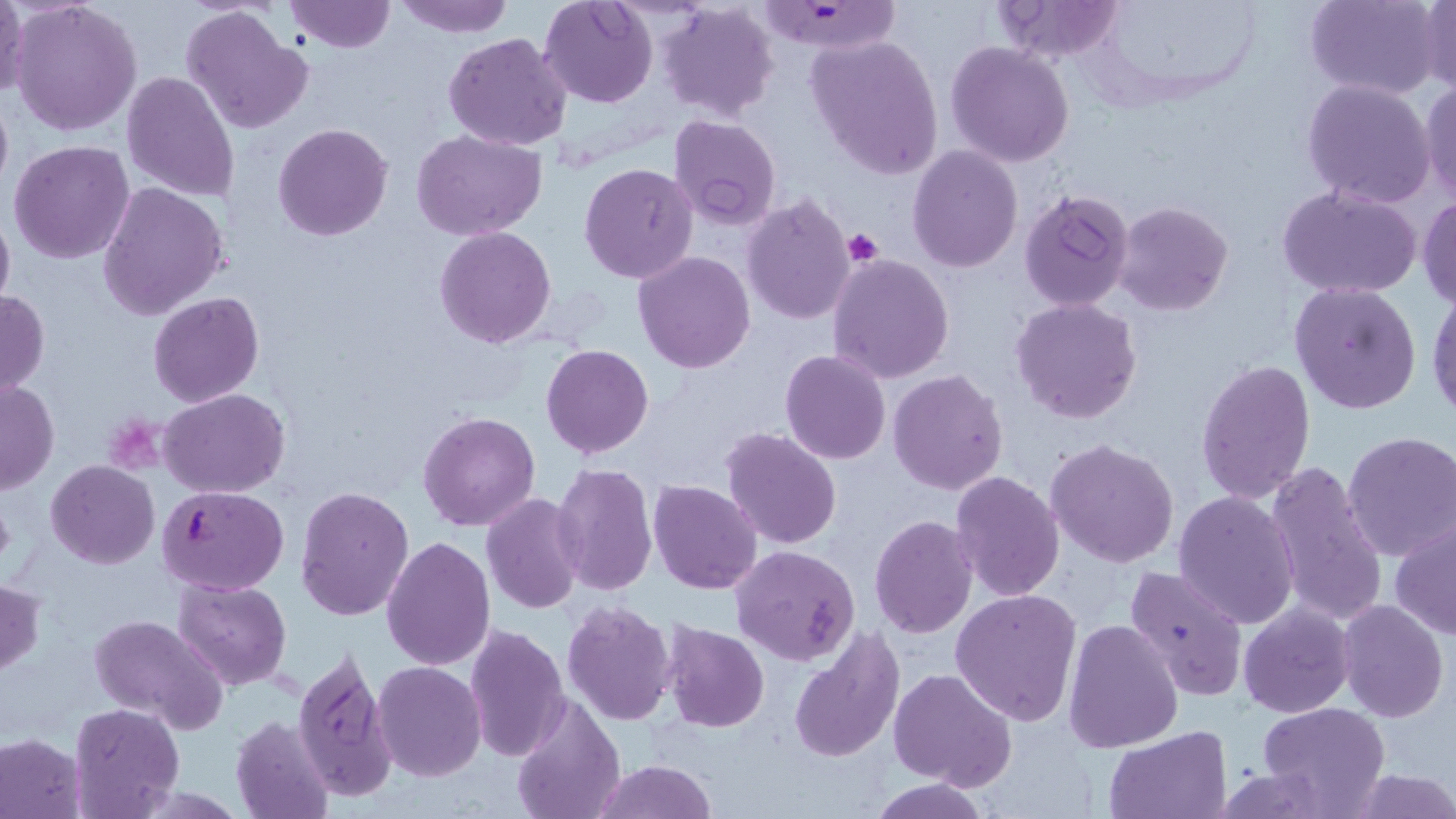
Summary:
  - Coordinate format: approximate bounding boxes as named x1/y1/x2/y2 corners in pixels
  - Plasmodium falciparum-infected red blood cell locations: (x1=755, y1=3, x2=906, y2=55), (x1=158, y1=485, x2=289, y2=595)
  - Platelet locations: (x1=843, y1=230, x2=883, y2=267)
  - Uninfected red blood cell locations: (x1=0, y1=0, x2=29, y2=101), (x1=9, y1=0, x2=142, y2=138), (x1=283, y1=0, x2=395, y2=53), (x1=394, y1=0, x2=513, y2=38), (x1=538, y1=0, x2=659, y2=109), (x1=992, y1=0, x2=1128, y2=62), (x1=1305, y1=0, x2=1443, y2=99), (x1=657, y1=1, x2=780, y2=121), (x1=1418, y1=1, x2=1455, y2=94), (x1=178, y1=7, x2=313, y2=135), (x1=443, y1=33, x2=572, y2=151), (x1=806, y1=34, x2=945, y2=179), (x1=946, y1=42, x2=1075, y2=168), (x1=122, y1=72, x2=240, y2=203), (x1=1302, y1=78, x2=1438, y2=207), (x1=1419, y1=79, x2=1456, y2=205), (x1=0, y1=83, x2=13, y2=201), (x1=668, y1=115, x2=781, y2=231), (x1=273, y1=123, x2=392, y2=241), (x1=598, y1=124, x2=746, y2=249), (x1=411, y1=128, x2=548, y2=240), (x1=8, y1=141, x2=133, y2=264), (x1=906, y1=146, x2=1024, y2=273), (x1=579, y1=162, x2=701, y2=283), (x1=98, y1=182, x2=228, y2=322), (x1=1276, y1=184, x2=1423, y2=300), (x1=1019, y1=188, x2=1135, y2=312), (x1=740, y1=192, x2=856, y2=325), (x1=1417, y1=195, x2=1456, y2=308), (x1=1113, y1=200, x2=1233, y2=315), (x1=0, y1=207, x2=14, y2=317), (x1=434, y1=226, x2=558, y2=348), (x1=633, y1=251, x2=756, y2=372), (x1=827, y1=253, x2=955, y2=384), (x1=1289, y1=282, x2=1421, y2=415), (x1=1426, y1=285, x2=1456, y2=421), (x1=0, y1=289, x2=48, y2=399), (x1=149, y1=293, x2=264, y2=407), (x1=1011, y1=297, x2=1143, y2=424), (x1=540, y1=344, x2=654, y2=458), (x1=780, y1=349, x2=891, y2=465), (x1=1195, y1=358, x2=1317, y2=505), (x1=889, y1=369, x2=1009, y2=495), (x1=1, y1=378, x2=58, y2=494), (x1=159, y1=387, x2=290, y2=496), (x1=417, y1=410, x2=540, y2=531), (x1=720, y1=426, x2=842, y2=548), (x1=1341, y1=431, x2=1456, y2=562), (x1=1046, y1=439, x2=1180, y2=568), (x1=659, y1=455, x2=824, y2=579), (x1=46, y1=460, x2=159, y2=568), (x1=1263, y1=461, x2=1388, y2=630), (x1=551, y1=462, x2=659, y2=596), (x1=951, y1=472, x2=1064, y2=600), (x1=647, y1=479, x2=763, y2=595), (x1=296, y1=485, x2=415, y2=621), (x1=1172, y1=491, x2=1300, y2=630), (x1=482, y1=494, x2=584, y2=613), (x1=868, y1=516, x2=978, y2=639), (x1=1390, y1=519, x2=1456, y2=640), (x1=383, y1=535, x2=496, y2=672), (x1=730, y1=545, x2=860, y2=667), (x1=1124, y1=564, x2=1251, y2=702), (x1=171, y1=577, x2=291, y2=691), (x1=0, y1=579, x2=46, y2=677), (x1=950, y1=589, x2=1082, y2=727), (x1=1338, y1=599, x2=1448, y2=721), (x1=561, y1=600, x2=677, y2=727), (x1=1238, y1=603, x2=1353, y2=718), (x1=87, y1=613, x2=227, y2=733), (x1=1064, y1=620, x2=1183, y2=753), (x1=662, y1=621, x2=769, y2=732), (x1=464, y1=623, x2=570, y2=764), (x1=789, y1=627, x2=904, y2=764), (x1=292, y1=646, x2=395, y2=800), (x1=373, y1=662, x2=487, y2=782), (x1=888, y1=667, x2=1018, y2=790), (x1=510, y1=694, x2=626, y2=819), (x1=69, y1=703, x2=185, y2=819), (x1=1259, y1=703, x2=1389, y2=816), (x1=230, y1=716, x2=334, y2=819), (x1=1103, y1=726, x2=1232, y2=819), (x1=0, y1=731, x2=87, y2=819), (x1=594, y1=759, x2=715, y2=819), (x1=1213, y1=767, x2=1337, y2=818), (x1=1348, y1=769, x2=1456, y2=818), (x1=867, y1=777, x2=992, y2=818)
  - Slide-level diagnosis: Plasmodium falciparum
  - Stain: May-Grünwald-Giemsa
  - Field of view: single
  - Image size: 1456×819 pixels
  - Preparation: thin blood smear
  - Modality: optical microscopy
  - Magnification: 1000x